Assess this cell for malaria.
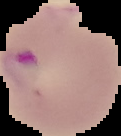
It is parasitized.

image type = segmented cell region with the area outside set to black
preparation = thin blood smear
image size = 121×136 pixels